Assess this cell for malaria.
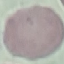
Uninfected.

capture = smartphone through the microscope eyepiece
stain = Giemsa
preparation = thin smear
image type = cell patch, automatically extracted from a larger field of view and resized to 64 × 64 pixels